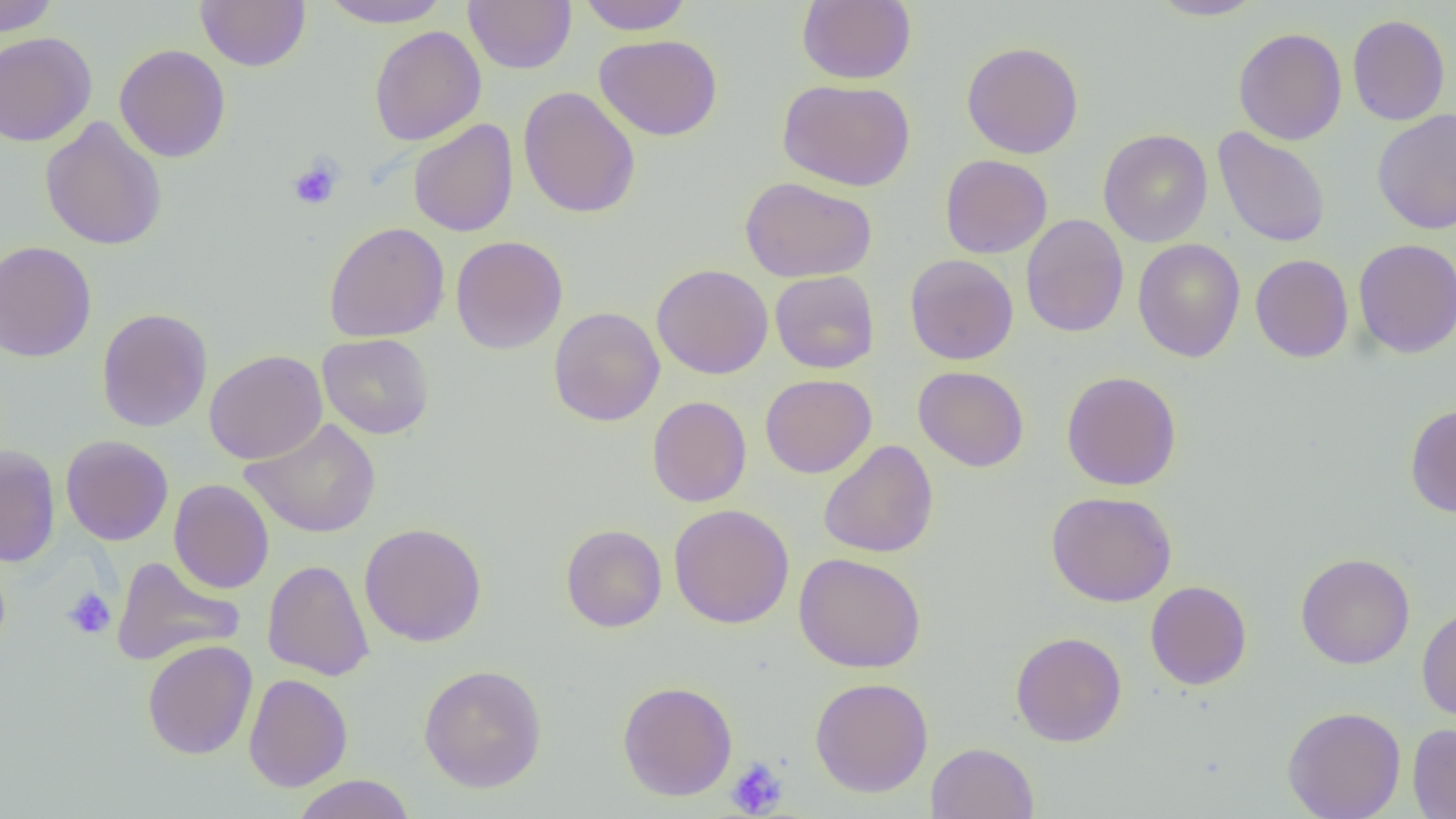
{
  "slide_level_diagnosis": "negative for blood parasites",
  "modality": "light microscopy",
  "uninfected_red_blood_cell_locations": "approximate bounding boxes as (x1, y1, x2, y2) in pixels: (0, 0, 60, 36), (195, 0, 311, 71), (318, 0, 453, 28), (463, 0, 576, 74), (576, 0, 694, 35), (797, 0, 916, 84), (1148, 0, 1266, 20), (1347, 14, 1450, 126), (369, 25, 486, 146), (1233, 27, 1347, 145), (0, 32, 96, 147), (594, 34, 723, 141), (961, 41, 1084, 158), (114, 44, 231, 162), (777, 79, 916, 191), (518, 87, 641, 219), (1371, 108, 1456, 234), (40, 116, 168, 251), (408, 119, 519, 237), (1212, 126, 1330, 248), (1098, 129, 1213, 247), (940, 154, 1053, 258), (740, 176, 876, 282), (1020, 214, 1129, 338), (323, 222, 450, 342), (450, 235, 567, 354), (1132, 238, 1246, 362), (1353, 238, 1456, 358), (0, 240, 97, 362), (904, 254, 1019, 365), (1250, 254, 1354, 362), (651, 264, 773, 379), (769, 270, 880, 374), (548, 306, 665, 427), (96, 307, 212, 432), (318, 333, 434, 439), (204, 350, 327, 464), (913, 366, 1030, 472), (1061, 370, 1182, 490), (760, 374, 877, 478), (647, 395, 752, 507), (1405, 403, 1456, 518), (241, 417, 381, 539), (60, 435, 174, 545), (817, 440, 939, 559), (0, 445, 61, 567), (168, 479, 274, 593), (1046, 490, 1177, 607), (669, 504, 794, 629), (359, 522, 487, 647), (560, 524, 667, 632), (793, 552, 926, 673), (1296, 552, 1415, 669), (112, 556, 245, 666), (262, 559, 375, 681), (1145, 580, 1252, 690), (1416, 606, 1456, 722), (1011, 631, 1127, 747), (141, 639, 257, 759), (418, 665, 547, 792), (243, 673, 352, 792), (810, 677, 933, 797), (617, 680, 738, 801), (1282, 706, 1406, 819), (1408, 723, 1456, 818), (925, 742, 1038, 819), (290, 774, 416, 819)",
  "magnification": "1000x",
  "platelet_locations": "approximate bounding boxes as (x1, y1, x2, y2) in pixels: (288, 158, 343, 210), (62, 586, 117, 640), (725, 758, 788, 817)",
  "image_size": "1456×819 pixels",
  "preparation": "thin blood film",
  "field_of_view": "one of a larger specimen"
}